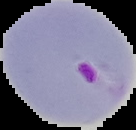

Image is 136×130 pixels. Cell region segmented out of the field of view; the surrounding area is masked to black. Malaria status: parasitized. From a thin blood film.